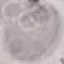

Malaria status: uninfected. Photographed with a smartphone camera at the microscope eyepiece. Cell patch, automatically extracted from a larger field of view and resized to 64 × 64 pixels. Thin blood smear. Giemsa stain.